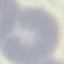

result: no malaria parasites seen
preparation: thin blood film
stain: Giemsa
capture: smartphone camera at the microscope eyepiece
image_type: automatically extracted cell patch, resized to 64 × 64 pixels